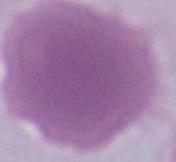

Summary:
  - Identification: erythrocyte
  - Modality: micrograph
  - Magnification: 1000x